Classify this cell by malaria status.
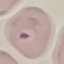

It is parasitized.

image type = cell patch, automatically extracted from a larger field of view and resized to 64 × 64 pixels
capture = smartphone camera at the microscope eyepiece
preparation = thin blood smear
stain = Giemsa